Classify this cell by malaria status.
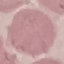
Uninfected.

Giemsa stain. Thin smear of blood. Automatically extracted cell patch, resized to 64 × 64 pixels. Photographed with a smartphone camera at the microscope eyepiece.